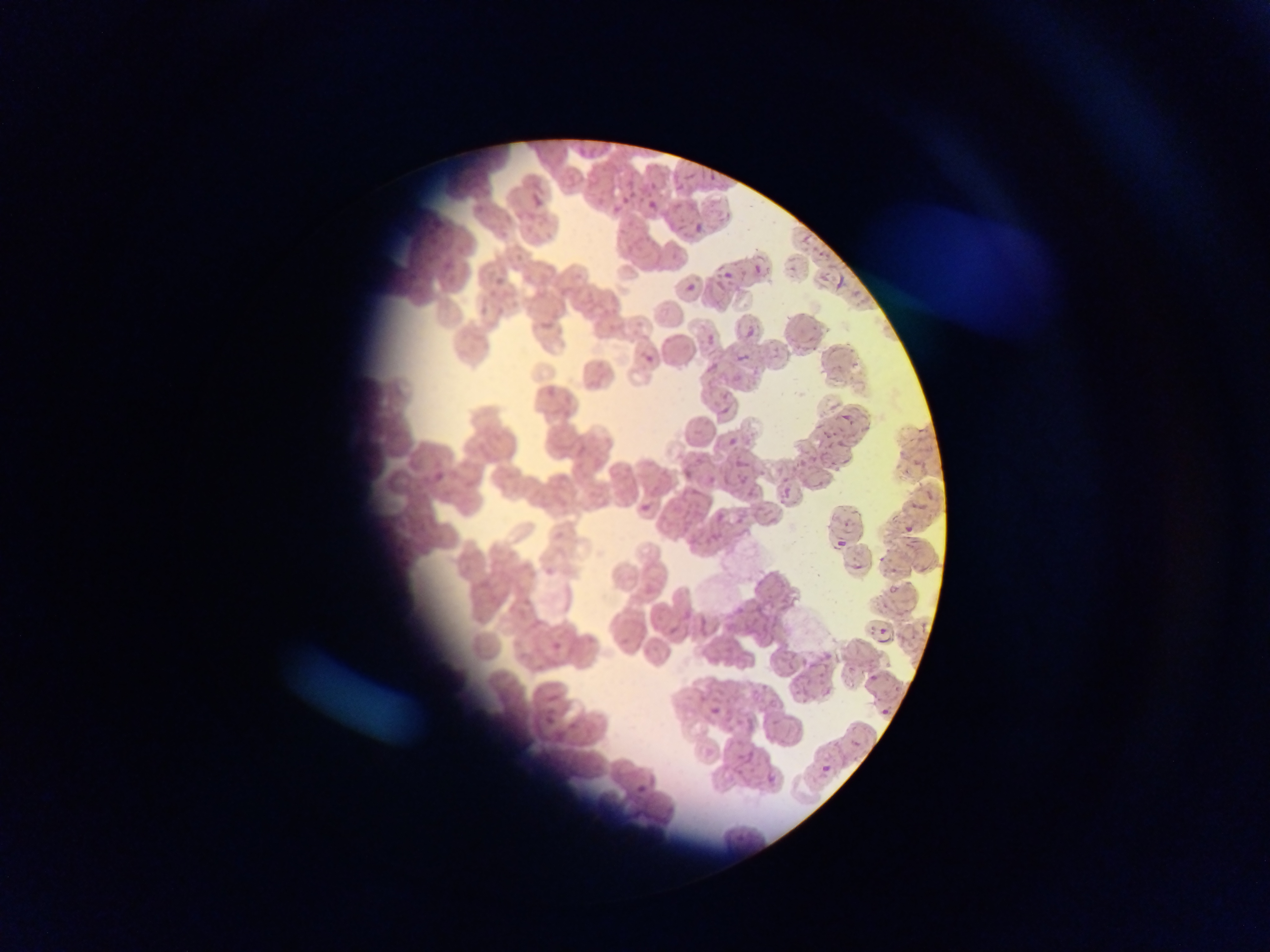
Approximate bounding boxes as left top right bottom in pixels.
Summary:
  - Malaria parasite locations: 709 172 715 182; 684 175 697 181; 652 181 659 193; 670 185 683 192; 534 194 541 207; 621 196 631 204; 647 200 656 209; 696 222 706 233; 674 224 684 229; 799 235 811 244; 720 272 735 279; 686 286 698 291; 744 328 754 339; 708 337 716 346; 738 353 749 361; 646 355 652 363; 710 362 718 371; 723 406 731 415; 839 416 849 421; 727 438 735 446; 838 457 849 465; 734 461 747 467; 785 489 789 501; 639 503 649 512; 716 513 725 520; 900 526 915 533; 837 541 846 548; 846 566 864 572; 890 568 896 576; 886 588 898 598; 875 635 892 644; 550 641 559 652; 865 675 876 684; 822 688 831 701; 770 699 777 712; 710 708 719 714; 881 710 889 716; 744 751 752 765; 818 764 831 776; 767 775 775 784; 633 785 646 794 | approximate x y pixel centers of objects too small to bound: 615 211; 757 269
  - Capture: mobile-phone photograph through a microscope
  - Preparation: thin blood film
  - Image size: 1270×952 pixels
  - Field of view: single
  - Country: Ghana